Assess this cell for malaria.
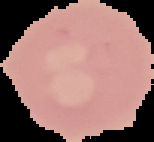
Uninfected.

Image is 154×142 pixels. From a thin blood smear. Cell region segmented out of the field of view; the surrounding area is masked to black.